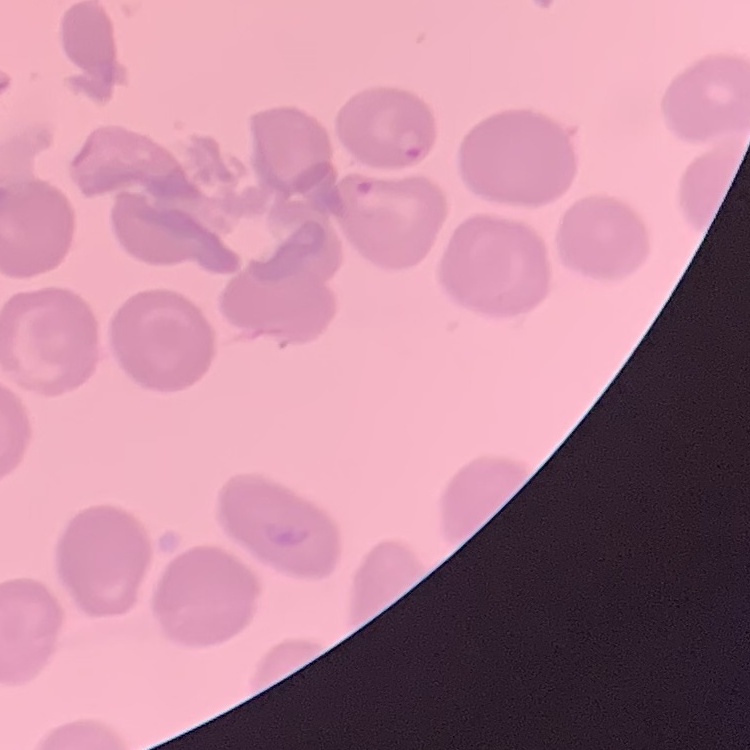 The red blood cells show no rouleaux formation. Stained with either Field's or Giemsa. One tile cut from a larger photomicrograph. Thin peripheral smear.